Describe the morphology of the red blood cells.
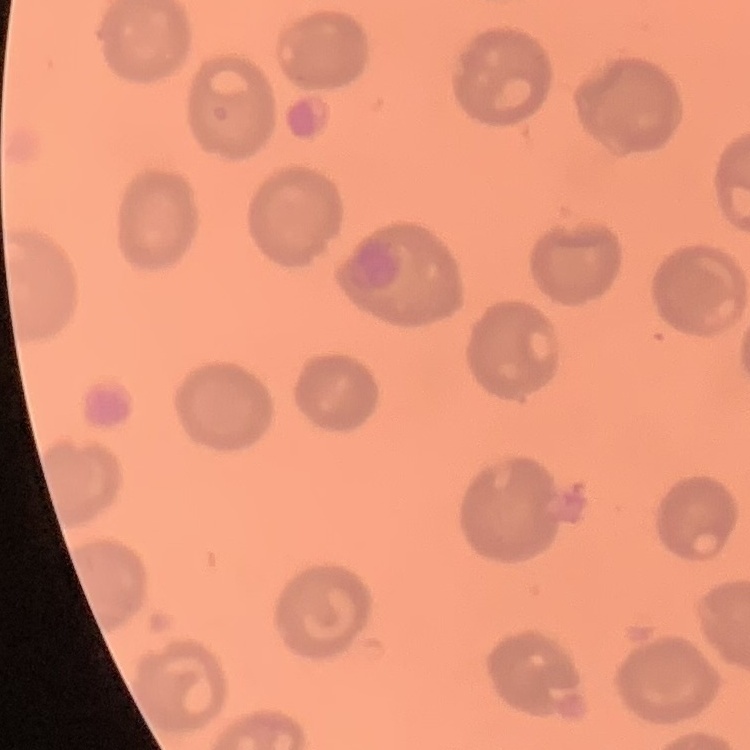

No rouleaux formation.

Square crop of a larger photomicrograph. Stained with either Field's or Giemsa. Thin blood smear.